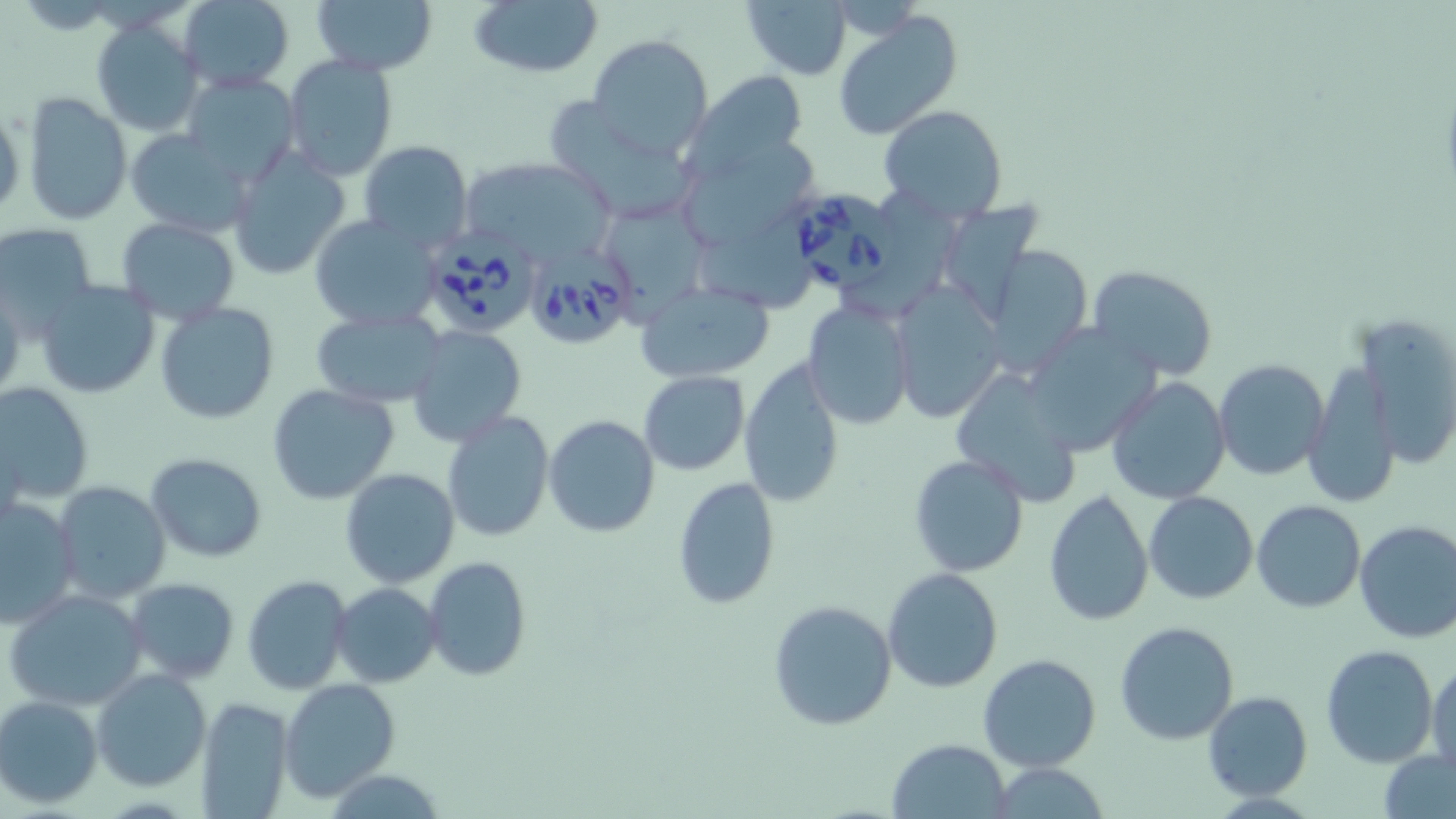
{
  "slide_level_diagnosis": "Babesia divergens",
  "stain": "May-Grünwald-Giemsa",
  "image_size": "1456×819 pixels",
  "modality": "light microscopy",
  "field_of_view": "one of a larger specimen",
  "preparation": "thin blood film",
  "uninfected_red_blood_cell_locations": "approximate bounding boxes as (x1, y1, x2, y2) in pixels: (175, 0, 294, 90), (311, 0, 437, 76), (466, 0, 604, 80), (741, 0, 854, 80), (833, 10, 963, 141), (91, 17, 207, 137), (585, 35, 713, 157), (282, 54, 398, 181), (687, 70, 810, 175), (181, 73, 300, 188), (21, 92, 133, 225), (549, 95, 691, 222), (1, 105, 25, 222), (878, 106, 1007, 222), (124, 128, 256, 236), (358, 141, 472, 251), (687, 144, 822, 246), (225, 147, 352, 281), (458, 158, 614, 264), (937, 204, 1043, 325), (611, 206, 713, 319), (308, 214, 442, 332), (116, 218, 240, 323), (704, 218, 819, 315), (0, 223, 97, 331), (983, 244, 1096, 374), (1086, 265, 1217, 381), (36, 278, 161, 401), (888, 280, 1008, 423), (635, 281, 776, 383), (801, 300, 914, 430), (155, 302, 278, 425), (312, 308, 448, 408), (1022, 321, 1162, 455), (1340, 322, 1456, 485), (406, 326, 526, 445), (1213, 359, 1329, 481), (738, 360, 843, 507), (1302, 361, 1401, 511), (951, 368, 1082, 504), (639, 371, 748, 476), (1105, 376, 1233, 505), (0, 382, 95, 504), (266, 382, 400, 505), (441, 409, 555, 542), (544, 415, 662, 538), (146, 453, 267, 562), (908, 454, 1030, 577), (339, 469, 460, 588), (671, 476, 780, 611), (52, 482, 172, 605), (1044, 490, 1154, 627), (1143, 492, 1258, 605), (0, 496, 80, 628), (1251, 500, 1365, 613), (1353, 520, 1456, 644), (424, 556, 531, 681), (881, 567, 1004, 694), (243, 575, 352, 694), (124, 577, 237, 682), (331, 583, 441, 687), (5, 587, 149, 711), (767, 599, 898, 733), (1114, 621, 1240, 746), (1319, 645, 1439, 768), (978, 653, 1104, 774), (1427, 661, 1456, 777), (93, 669, 211, 791), (280, 678, 400, 800), (1203, 691, 1314, 802), (195, 695, 294, 818), (0, 696, 103, 807), (886, 738, 1012, 818), (1380, 751, 1456, 819), (984, 762, 1114, 818)",
  "magnification": "1000x",
  "babesia_divergens_infected_red_blood_cell_locations": "approximate bounding boxes as (x1, y1, x2, y2) in pixels: (785, 187, 898, 288), (419, 229, 541, 337), (520, 243, 636, 347)"
}